Assess this cell for malaria.
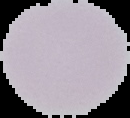
Uninfected.

preparation: thin blood film
image_size: 130×118 pixels
image_type: cell region segmented out of the field of view; surrounding area masked to black